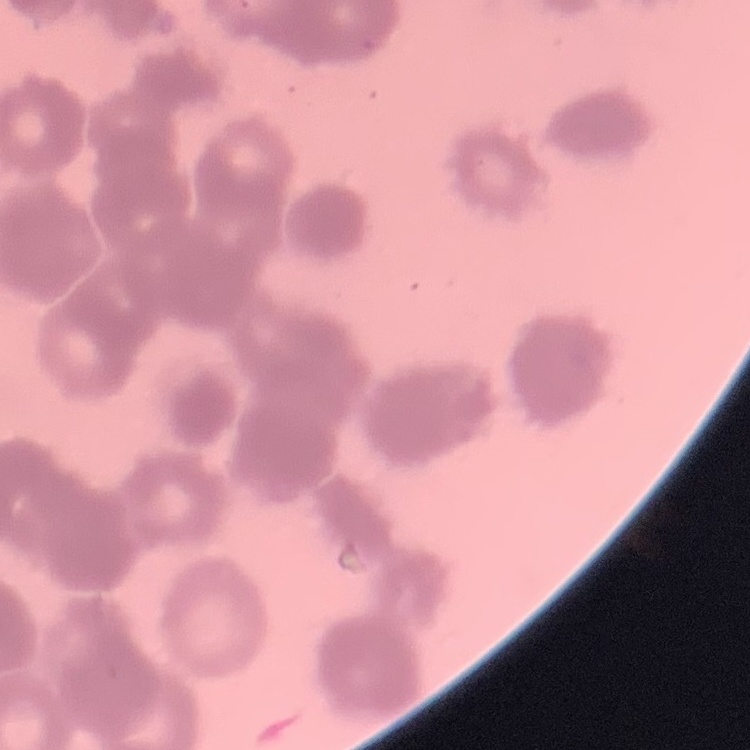

red blood cell morphology = rouleaux formation
preparation = thin blood film
image type = square crop of a larger photomicrograph
stain = Field's or Giemsa